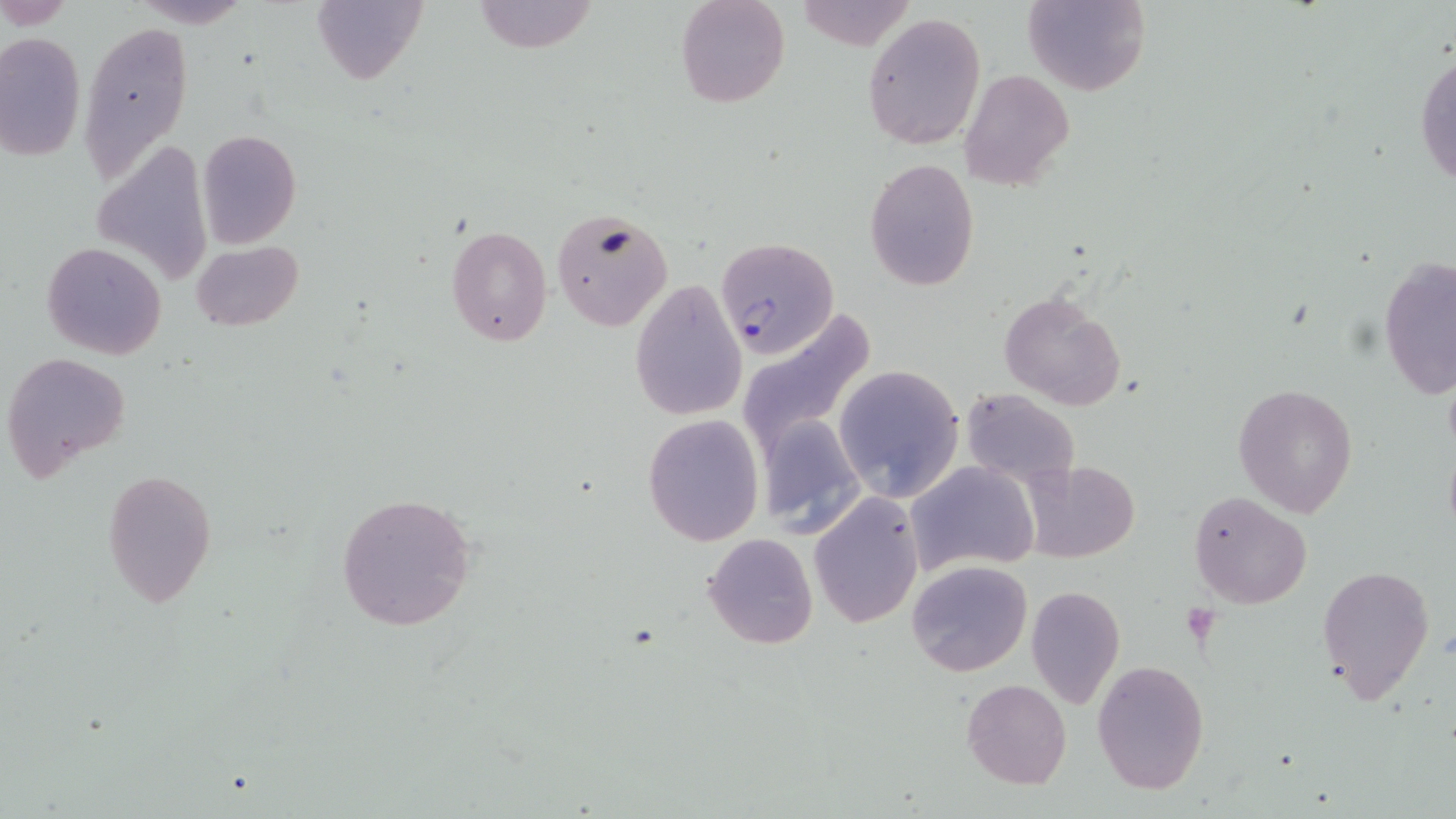

slide-level diagnosis = Plasmodium falciparum
uninfected red blood cell locations = approximate bounding boxes as named x1/y1/x2/y2 corners in pixels: (x1=311, y1=0, x2=427, y2=86), (x1=473, y1=0, x2=600, y2=54), (x1=677, y1=0, x2=789, y2=108), (x1=1023, y1=0, x2=1150, y2=96), (x1=863, y1=12, x2=986, y2=150), (x1=77, y1=19, x2=191, y2=185), (x1=0, y1=30, x2=86, y2=163), (x1=1415, y1=46, x2=1456, y2=193), (x1=959, y1=68, x2=1073, y2=193), (x1=195, y1=128, x2=302, y2=248), (x1=89, y1=139, x2=214, y2=285), (x1=864, y1=158, x2=979, y2=290), (x1=550, y1=206, x2=672, y2=331), (x1=445, y1=224, x2=552, y2=347), (x1=191, y1=239, x2=303, y2=333), (x1=42, y1=241, x2=167, y2=360), (x1=1377, y1=256, x2=1454, y2=403), (x1=629, y1=279, x2=749, y2=420), (x1=998, y1=289, x2=1128, y2=409), (x1=736, y1=310, x2=878, y2=454), (x1=1, y1=351, x2=131, y2=482), (x1=832, y1=365, x2=963, y2=502), (x1=1233, y1=383, x2=1358, y2=518), (x1=961, y1=389, x2=1080, y2=487), (x1=756, y1=411, x2=868, y2=537), (x1=642, y1=413, x2=765, y2=546), (x1=907, y1=460, x2=1038, y2=577), (x1=1023, y1=460, x2=1137, y2=561), (x1=101, y1=468, x2=218, y2=610), (x1=1189, y1=491, x2=1310, y2=608), (x1=336, y1=492, x2=477, y2=631), (x1=808, y1=492, x2=924, y2=628), (x1=702, y1=533, x2=818, y2=650), (x1=907, y1=559, x2=1033, y2=678), (x1=1316, y1=564, x2=1435, y2=704), (x1=1024, y1=586, x2=1126, y2=709), (x1=1093, y1=660, x2=1210, y2=796), (x1=960, y1=679, x2=1072, y2=789)
preparation = thin blood smear
field of view = one of a larger specimen
Plasmodium falciparum-infected red blood cell locations = approximate bounding boxes as named x1/y1/x2/y2 corners in pixels: (x1=717, y1=237, x2=838, y2=358)
modality = light microscopy
magnification = 1000x
stain = May-Grünwald-Giemsa
image size = 1456×819 pixels